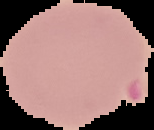

preparation = thin blood film
image type = segmented cell region on a black background
result = Plasmodium parasites identified
image size = 154×130 pixels